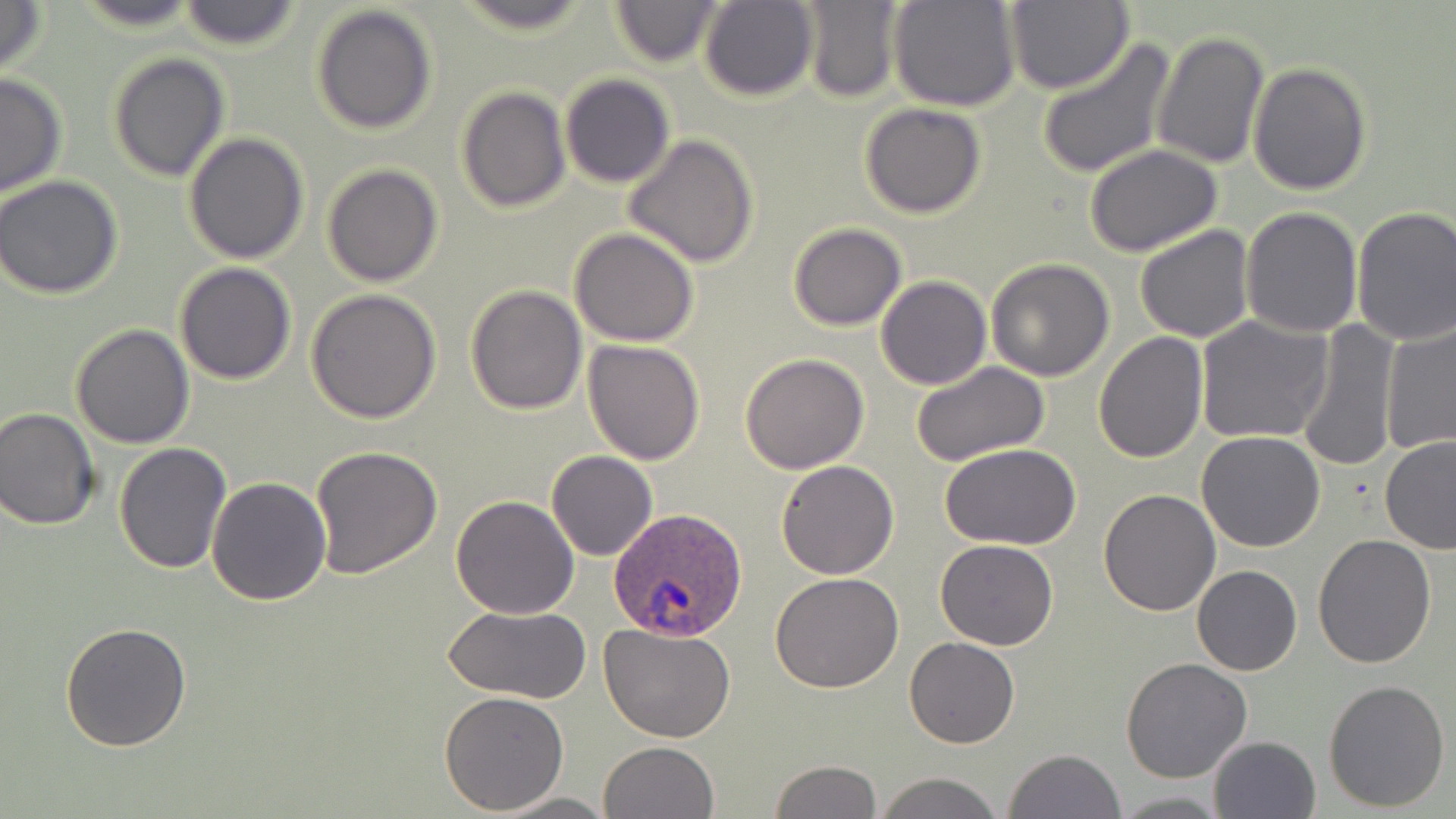
Summary:
  - Coordinate format: approximate bounding boxes as named x1/y1/x2/y2 corners in pixels
  - Uninfected red blood cell locations: (x1=72, y1=0, x2=205, y2=30), (x1=178, y1=0, x2=301, y2=51), (x1=448, y1=0, x2=601, y2=36), (x1=606, y1=0, x2=726, y2=67), (x1=0, y1=1, x2=48, y2=82), (x1=698, y1=1, x2=818, y2=102), (x1=795, y1=1, x2=902, y2=101), (x1=889, y1=1, x2=1021, y2=112), (x1=1005, y1=1, x2=1133, y2=95), (x1=310, y1=4, x2=438, y2=136), (x1=1152, y1=29, x2=1269, y2=168), (x1=1036, y1=38, x2=1175, y2=178), (x1=107, y1=52, x2=230, y2=182), (x1=1248, y1=61, x2=1371, y2=195), (x1=0, y1=72, x2=68, y2=198), (x1=560, y1=74, x2=674, y2=188), (x1=457, y1=86, x2=571, y2=212), (x1=859, y1=103, x2=986, y2=218), (x1=184, y1=133, x2=311, y2=265), (x1=623, y1=133, x2=762, y2=268), (x1=1084, y1=146, x2=1224, y2=256), (x1=321, y1=165, x2=443, y2=287), (x1=0, y1=176, x2=125, y2=301), (x1=1351, y1=205, x2=1456, y2=346), (x1=1241, y1=207, x2=1366, y2=338), (x1=786, y1=222, x2=908, y2=331), (x1=1134, y1=225, x2=1255, y2=344), (x1=570, y1=228, x2=698, y2=348), (x1=985, y1=259, x2=1116, y2=381), (x1=174, y1=262, x2=298, y2=384), (x1=876, y1=275, x2=991, y2=390), (x1=464, y1=283, x2=588, y2=414), (x1=306, y1=290, x2=442, y2=426), (x1=1195, y1=315, x2=1331, y2=445), (x1=1293, y1=320, x2=1404, y2=472), (x1=1380, y1=321, x2=1456, y2=455), (x1=70, y1=323, x2=196, y2=448), (x1=1094, y1=331, x2=1209, y2=464), (x1=583, y1=340, x2=706, y2=465), (x1=740, y1=353, x2=870, y2=474), (x1=910, y1=360, x2=1051, y2=467), (x1=1, y1=408, x2=101, y2=530), (x1=1197, y1=431, x2=1327, y2=551), (x1=1379, y1=435, x2=1456, y2=553), (x1=114, y1=441, x2=232, y2=574), (x1=940, y1=443, x2=1084, y2=548), (x1=309, y1=445, x2=441, y2=579), (x1=546, y1=451, x2=658, y2=561), (x1=775, y1=459, x2=900, y2=579), (x1=206, y1=478, x2=332, y2=605), (x1=1097, y1=487, x2=1221, y2=615), (x1=450, y1=495, x2=579, y2=619), (x1=1311, y1=535, x2=1436, y2=668), (x1=934, y1=538, x2=1059, y2=651), (x1=1192, y1=564, x2=1302, y2=676), (x1=770, y1=571, x2=905, y2=694), (x1=442, y1=605, x2=590, y2=703), (x1=61, y1=621, x2=193, y2=753), (x1=599, y1=621, x2=736, y2=742), (x1=904, y1=638, x2=1019, y2=749), (x1=1120, y1=657, x2=1252, y2=784), (x1=1323, y1=678, x2=1451, y2=813), (x1=438, y1=690, x2=569, y2=813), (x1=1208, y1=735, x2=1321, y2=819), (x1=598, y1=741, x2=720, y2=819), (x1=1004, y1=748, x2=1127, y2=819), (x1=770, y1=760, x2=881, y2=818), (x1=874, y1=773, x2=1005, y2=819), (x1=494, y1=792, x2=614, y2=818), (x1=1110, y1=792, x2=1228, y2=816)
  - Plasmodium ovale-infected red blood cell locations: (x1=609, y1=508, x2=746, y2=644)
  - Slide-level diagnosis: Plasmodium ovale
  - Field of view: one of a larger specimen
  - Magnification: 1000x
  - Stain: May-Grünwald-Giemsa
  - Modality: optical microscopy
  - Image size: 1456×819 pixels
  - Preparation: thin blood film